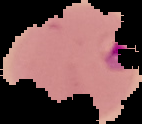
image type = cell region segmented out of the field of view; surrounding area masked to black
preparation = thin blood smear
image size = 142×124 pixels
malaria status = parasitized